Name the parasite shown.
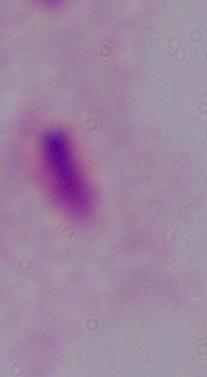
This is a trichomonad.

1000x magnification. Micrograph.